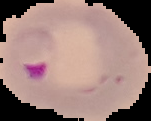
preparation = thin blood film
result = malaria parasites identified
image size = 151×121 pixels
image type = segmented cell region on a black background